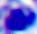

{
  "identification": "white blood cell",
  "magnification": "400x",
  "modality": "photomicrograph"
}